Identify the cell.
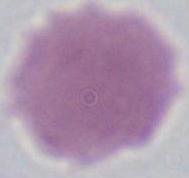
This is an erythrocyte.

Summary:
  - Modality: micrograph
  - Magnification: 1000x